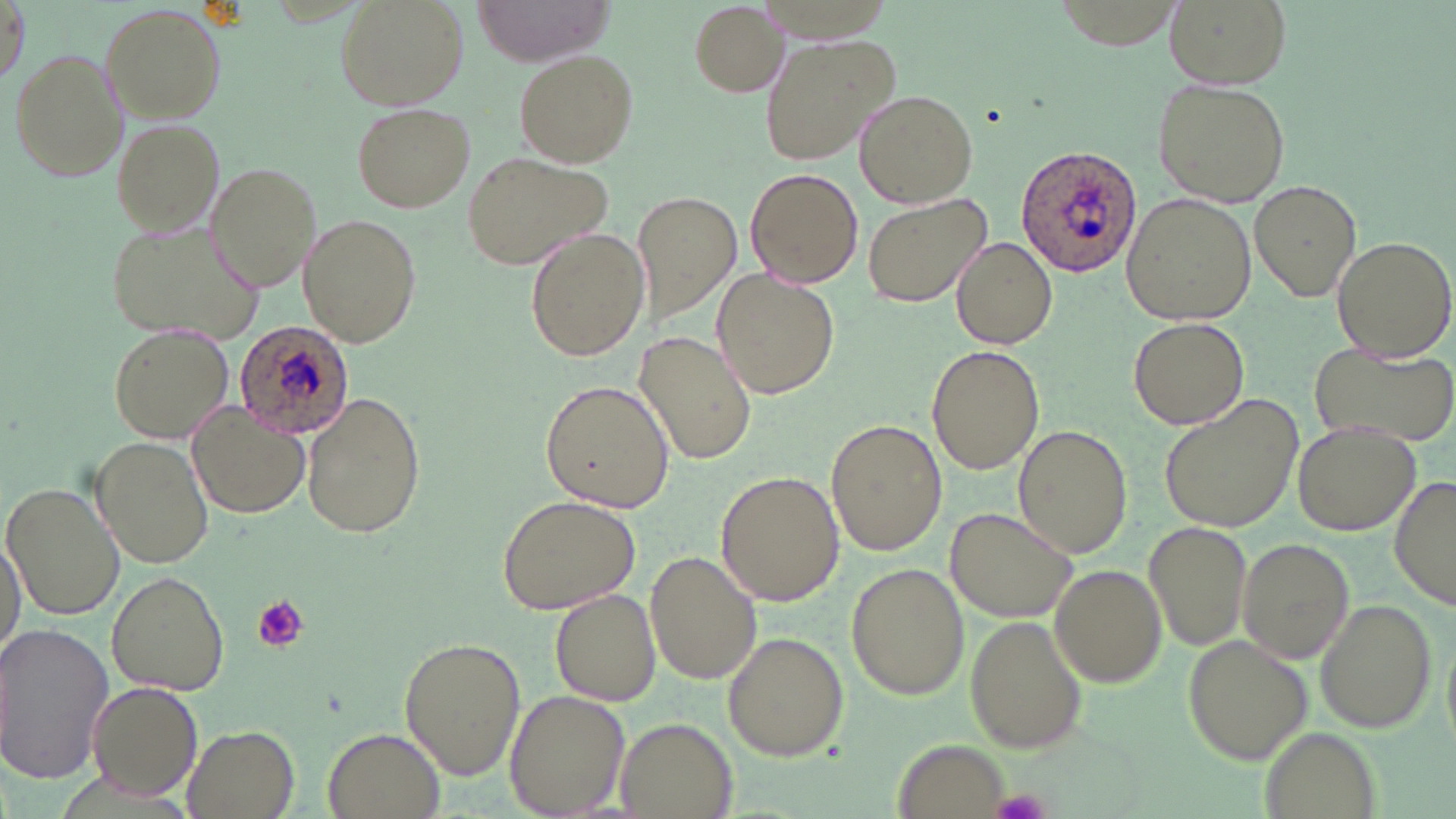
{
  "slide_level_diagnosis": "Plasmodium ovale",
  "image_size": "1456×819 pixels",
  "modality": "optical microscopy",
  "uninfected_red_blood_cell_locations": "approximate bounding boxes as (x1,y1)-(x2,y2) corner pairs in pixels: (2,0)-(28,87), (335,0)-(468,110), (470,0)-(614,67), (1165,0)-(1287,89), (687,2)-(790,97), (101,3)-(226,121), (758,34)-(898,166), (9,49)-(127,183), (514,49)-(636,167), (1152,79)-(1290,206), (853,89)-(978,208), (351,103)-(475,212), (109,117)-(225,238), (461,150)-(615,271), (205,161)-(322,292), (743,168)-(863,289), (1248,182)-(1361,300), (630,190)-(741,328), (863,193)-(991,308), (1124,193)-(1256,326), (298,213)-(420,347), (105,220)-(268,345), (524,228)-(649,363), (950,235)-(1058,349), (1330,235)-(1455,361), (710,268)-(840,399), (1129,318)-(1249,429), (110,325)-(233,443), (635,332)-(758,465), (1309,343)-(1456,449), (926,346)-(1044,475), (540,381)-(673,512), (301,388)-(426,539), (1157,393)-(1304,536), (185,404)-(308,519), (827,419)-(947,556), (1291,420)-(1420,536), (1014,425)-(1130,557), (95,435)-(214,569), (715,470)-(844,609), (1391,472)-(1454,617), (3,480)-(124,621), (497,495)-(641,613), (947,507)-(1078,623), (1143,519)-(1255,656), (1,528)-(26,663), (1238,538)-(1355,662), (643,551)-(762,685), (1047,565)-(1166,690), (847,566)-(969,701), (107,570)-(230,695), (551,588)-(661,706), (1313,597)-(1437,733), (968,613)-(1086,753), (0,624)-(116,787), (721,631)-(848,761), (1185,633)-(1314,764), (400,638)-(526,777), (87,682)-(202,802), (506,690)-(627,818), (615,716)-(739,819), (183,725)-(300,819), (324,730)-(444,818), (891,739)-(1012,819)",
  "stain": "May-Grünwald-Giemsa",
  "plasmodium_ovale_infected_red_blood_cell_locations": "approximate bounding boxes as (x1,y1)-(x2,y2) corner pairs in pixels: (1017,144)-(1141,278), (234,322)-(357,439)",
  "magnification": "1000x",
  "field_of_view": "one of a larger specimen",
  "preparation": "thin blood smear",
  "platelet_locations": "approximate bounding boxes as (x1,y1)-(x2,y2) corner pairs in pixels: (251,595)-(308,651)"
}